Assess this cell for malaria.
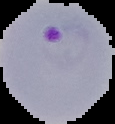
Parasitized.

Summary:
  - Image size: 115×124 pixels
  - Preparation: thin blood film
  - Image type: segmented cell region on a black background